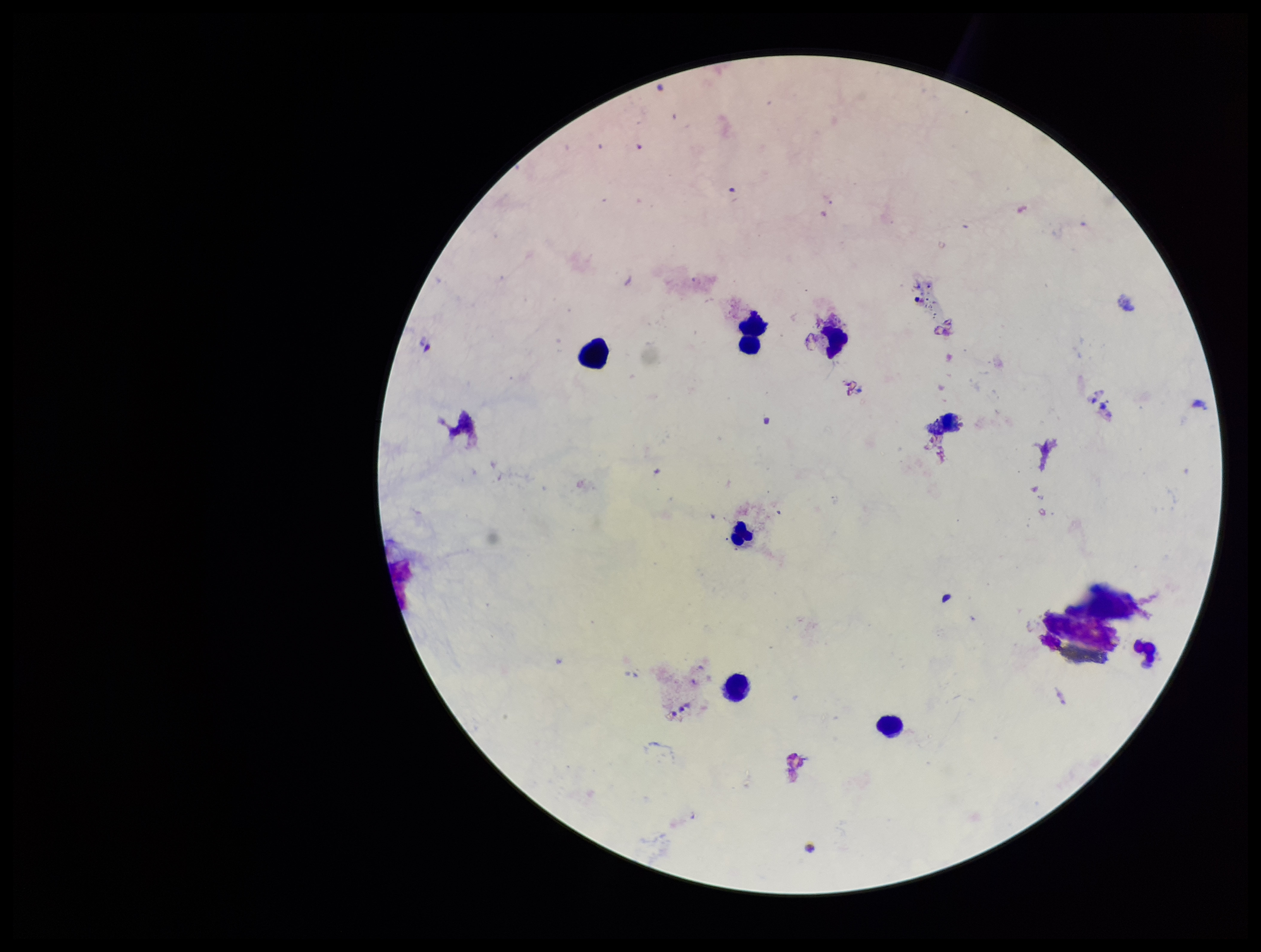 Single field of view. Image is 1261×952 pixels. Parasite count: 0. Leukocyte count: 6. Stained with Giemsa. Photographed through the microscope eyepiece with a smartphone camera. Preparation: thick smear. Patient malaria status: negative. Plasmodium parasites: none detected.